Report the malaria status of this cell.
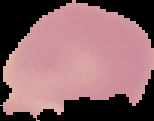

It is uninfected.

Cell region segmented out of the field of view; the surrounding area is masked to black. From a thin blood smear. Image is 154×121 pixels.